Report the malaria status of this cell.
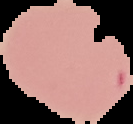

It is uninfected.

image type = cell region segmented out of the field of view; surrounding area masked to black
image size = 133×124 pixels
preparation = thin blood smear